Identify the parasite.
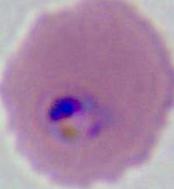

Plasmodium.

Summary:
  - Modality: photomicrograph
  - Magnification: 400x or 1000x